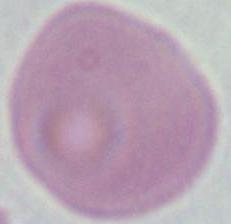
1000x magnification. Micrograph. An erythrocyte is seen.